State the preparation type.
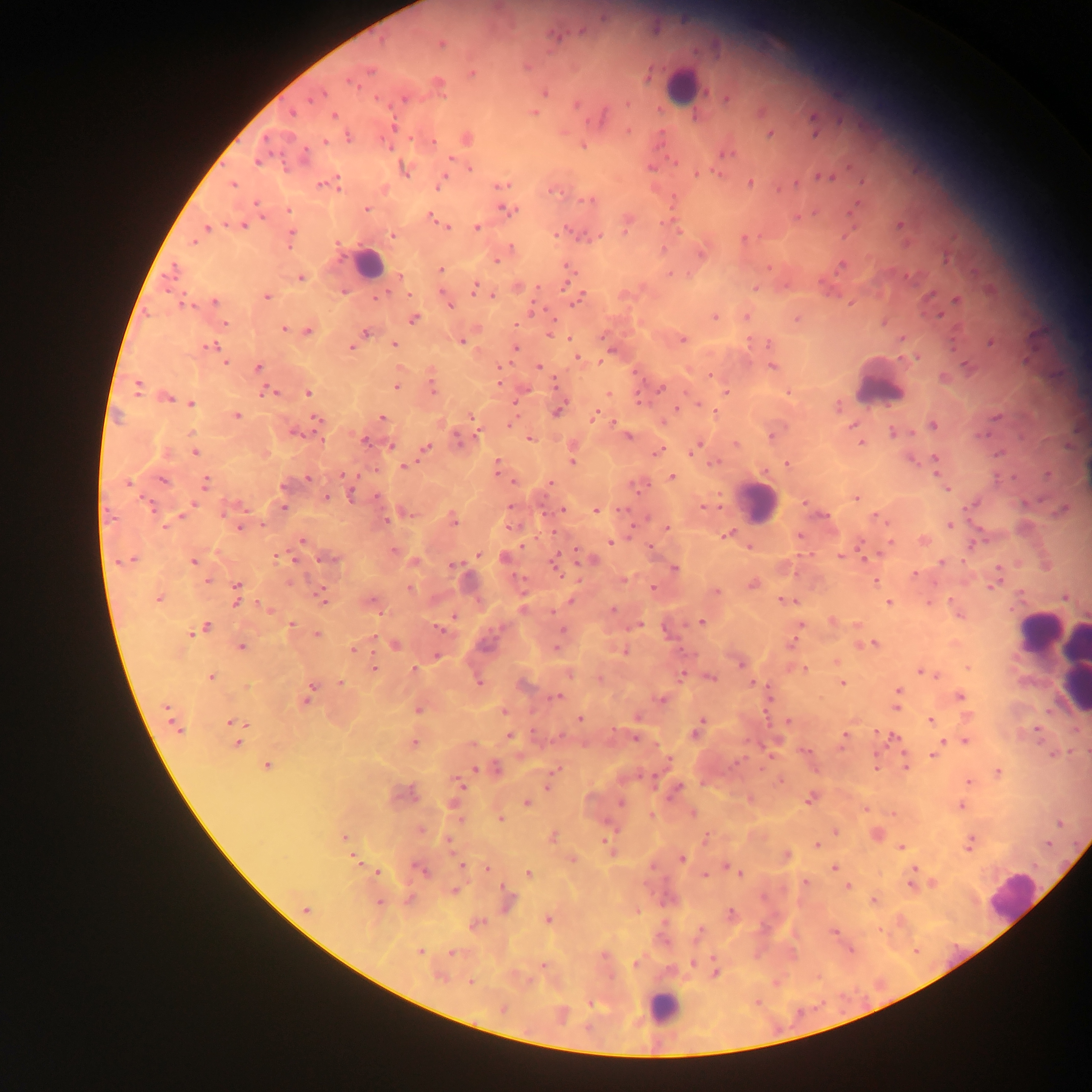
Thick blood smear.

Plasmodium parasite locations = approximate centers as [x, y] in pixels: [441, 43], [369, 70], [472, 73], [437, 84], [545, 91], [317, 95], [292, 112], [533, 113], [334, 115], [392, 126], [770, 133], [348, 137], [465, 138], [324, 142], [583, 145], [727, 153], [257, 160], [404, 168], [470, 168], [697, 173], [822, 177], [443, 180], [333, 181], [326, 183], [750, 183], [232, 184], [501, 184], [553, 189], [586, 200], [366, 209], [508, 209], [289, 210], [431, 216], [797, 217], [627, 221], [899, 224], [243, 225], [444, 225], [447, 226], [206, 227], [477, 227], [391, 235], [291, 237], [743, 238], [194, 241], [510, 247], [701, 254], [496, 259], [841, 265], [439, 269], [567, 269], [399, 276], [301, 278], [474, 287], [517, 287], [755, 288], [409, 295], [492, 295], [376, 296], [265, 297], [578, 299], [956, 299], [446, 300], [214, 302], [183, 303], [747, 315], [715, 316], [413, 318], [797, 318], [224, 323], [284, 329], [307, 330], [364, 331], [549, 332], [902, 337], [682, 339], [461, 341], [991, 341], [768, 343], [394, 344], [208, 346], [352, 347], [516, 348], [577, 357], [917, 357], [225, 361], [600, 361], [538, 366], [772, 366], [258, 368], [499, 368], [710, 375], [499, 382], [137, 386], [396, 386], [432, 386], [660, 388], [268, 392], [307, 392], [726, 392], [788, 392], [608, 393], [165, 397], [191, 404], [699, 404], [837, 405], [558, 408], [676, 408], [715, 413], [237, 416], [595, 416], [382, 417], [472, 418], [318, 421], [613, 422], [511, 423], [932, 425], [853, 426], [295, 432], [894, 432], [627, 435], [772, 435], [530, 438], [459, 439], [364, 440], [860, 442], [736, 444], [389, 445], [696, 446], [573, 447], [424, 448], [657, 450], [195, 452], [572, 459], [715, 463], [787, 463], [936, 463], [404, 466], [497, 466], [1048, 474], [672, 477], [308, 478], [162, 481], [514, 481], [549, 482], [129, 483], [205, 483], [284, 484], [638, 485], [946, 489], [352, 494], [326, 497], [856, 498], [804, 502], [973, 503], [283, 506], [702, 506], [230, 508], [562, 509], [596, 509], [1063, 510], [406, 512], [823, 516], [877, 517], [452, 519], [950, 524], [239, 526], [512, 526], [666, 527], [726, 535], [799, 535], [301, 540], [923, 541], [610, 542], [861, 543], [974, 543], [749, 548], [393, 550], [478, 554], [840, 555], [505, 557], [329, 559], [591, 559], [130, 560], [193, 561], [414, 561], [941, 562], [556, 564], [453, 565], [673, 569], [915, 575], [996, 579], [207, 580], [623, 580], [875, 581], [752, 584], [409, 588], [652, 588], [715, 591], [237, 593], [320, 596], [1066, 596], [158, 598], [572, 600], [784, 600], [888, 602], [370, 603], [928, 603], [523, 607], [612, 609], [832, 620], [701, 622], [290, 625], [800, 625], [857, 625], [636, 626], [199, 629], [440, 629], [316, 634], [791, 643], [873, 643], [395, 644], [241, 646], [557, 646], [353, 649], [623, 650], [437, 655], [836, 661], [739, 662], [968, 667], [803, 668], [374, 669], [414, 669], [921, 671], [568, 673], [682, 673], [928, 673], [709, 676], [210, 677], [478, 681], [842, 682], [341, 683], [753, 683], [522, 685], [898, 690], [307, 694], [557, 697], [959, 697], [660, 698], [896, 698], [895, 707], [418, 709], [503, 711], [966, 715], [579, 719], [930, 720], [172, 721], [788, 721], [233, 722], [697, 729], [1036, 729], [509, 736], [844, 736], [636, 737], [893, 737], [941, 740], [965, 741], [237, 742], [414, 742], [472, 744], [804, 751], [933, 754], [668, 760], [266, 765], [905, 766], [875, 767], [494, 768], [556, 769], [998, 772], [780, 779], [969, 781], [458, 784], [548, 784], [675, 789], [402, 794], [811, 797], [527, 803], [961, 805], [456, 808], [865, 809], [692, 813], [892, 813], [650, 815], [500, 819], [1060, 822], [420, 829], [835, 832], [876, 834], [552, 836], [344, 838], [705, 838], [447, 842], [969, 843], [1047, 843], [816, 845], [608, 847], [901, 847], [785, 856], [354, 858], [572, 859], [682, 859], [727, 864], [461, 865], [833, 867], [488, 868], [420, 869], [731, 869], [914, 869], [376, 872], [740, 873], [528, 874], [704, 875], [805, 882], [932, 883], [910, 885], [847, 886], [454, 890], [507, 899], [874, 900], [379, 902], [306, 908], [731, 915], [547, 919], [476, 923], [833, 931], [698, 932], [849, 949], [419, 951], [452, 952], [635, 963], [693, 963], [542, 964], [715, 971], [440, 975], [470, 982], [502, 1008], [561, 1014]
capture = mobile-phone photograph through a microscope
leukocyte locations = approximate centers as [x, y] in pixels: [680, 85], [369, 264], [880, 383], [758, 502], [1038, 631], [1052, 651], [1070, 666], [1076, 688], [1012, 896], [663, 1007]
field of view = single
country = Ghana
image size = 1092×1092 pixels